Comment on the morphology of the erythrocytes.
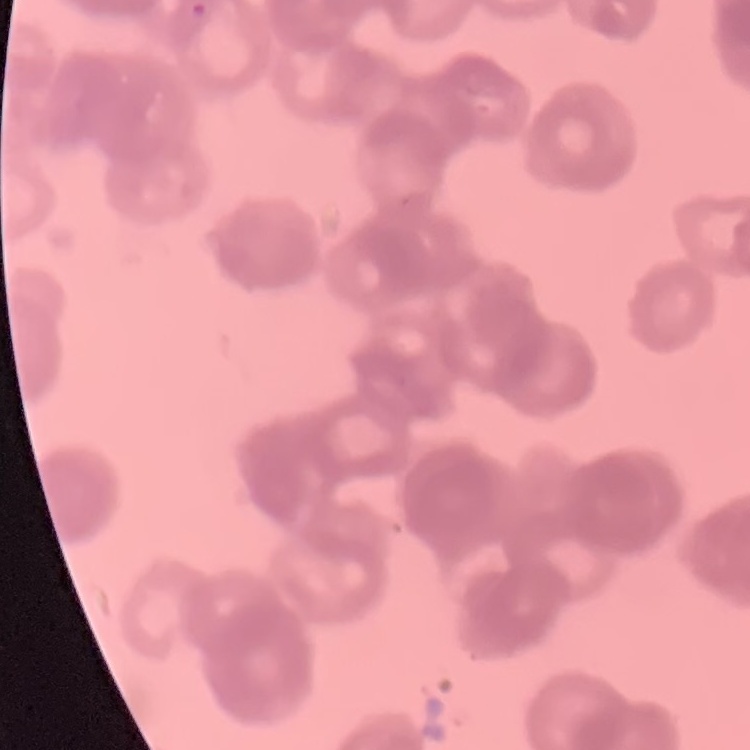

They show rouleaux formation.

Stained with either Field's or Giemsa. One tile cut from a larger photomicrograph. Thin blood film.